Give the position of every Plasmodium parasite.
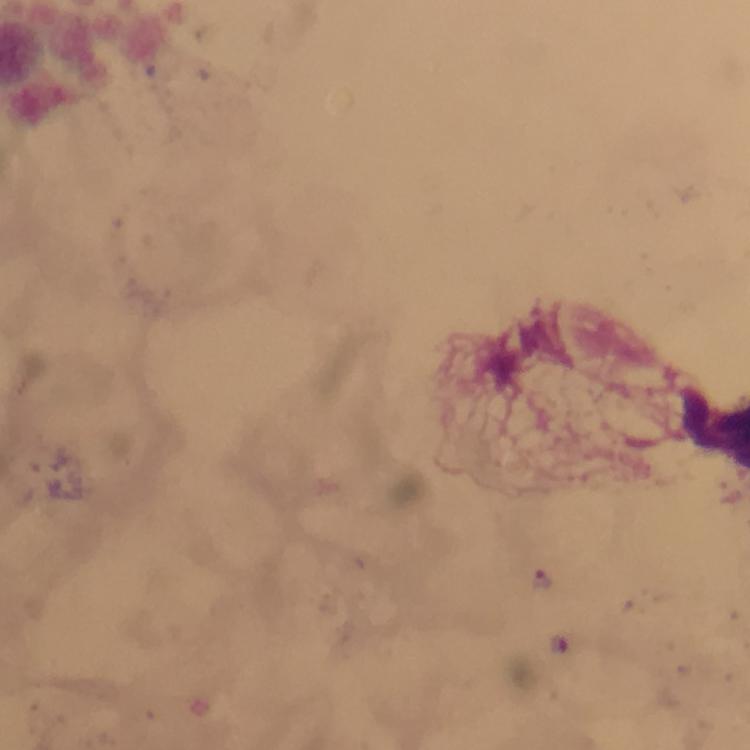
Approximate centers as (x, y) in pixels.
Plasmodium parasites: (542, 580).

A crop from one field of view. Giemsa-stained preparation. Immersion oil was used. From a diagnostic examination for malaria. Photographed through the microscope with a smartphone camera. At 100x magnification. Image is 750×750 pixels. Thick blood smear.